Assess this cell for malaria.
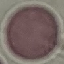

Uninfected.

Thin blood film. Photographed with a smartphone camera at the microscope eyepiece. Giemsa stain. Cell patch, automatically extracted from a larger field of view and resized to 64 × 64 pixels.